Name the parasite shown.
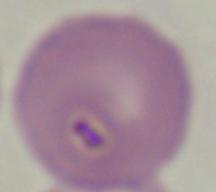

This is Babesia.

Summary:
  - Modality: micrograph
  - Magnification: 1000x